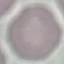
Summary:
  - Malaria status: uninfected
  - Preparation: thin blood smear
  - Image type: automatically extracted cell patch, resized to 64 × 64 pixels
  - Stain: Giemsa
  - Capture: smartphone camera at the microscope eyepiece